Assess the morphology of the erythrocytes.
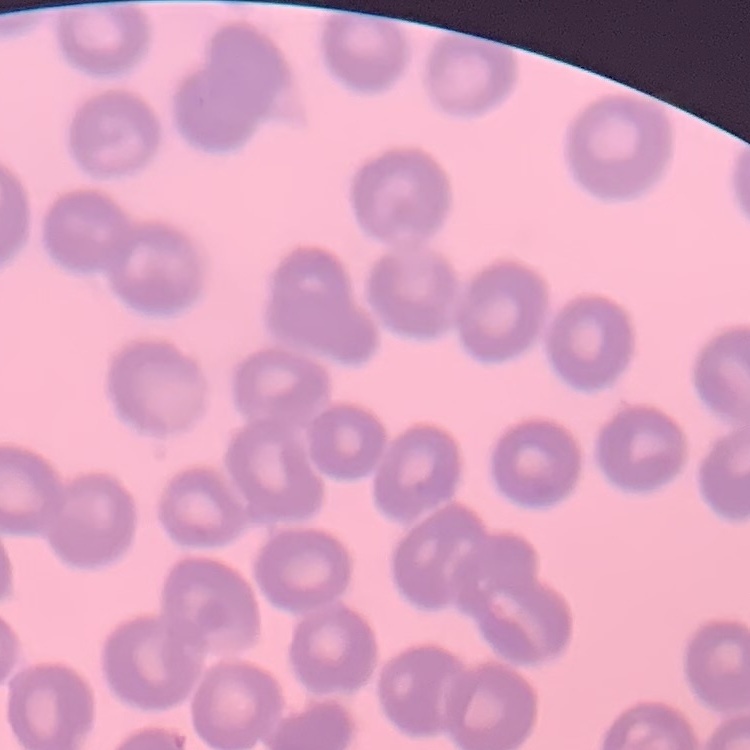

They show no rouleaux formation.

Summary:
  - Preparation: thin blood film
  - Image type: square crop of a larger photomicrograph
  - Stain: Field's or Giemsa